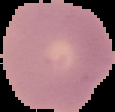
Image is 115×112 pixels. Result: negative for Plasmodium parasites. From a thin blood film. Cell region segmented out of the field of view; the surrounding area is masked to black.